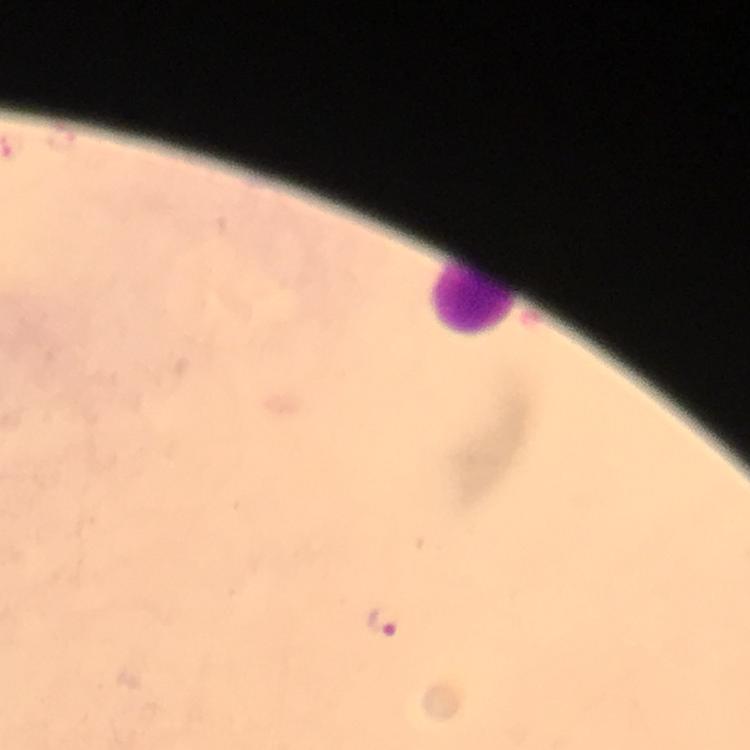

{
  "cropped_from": "one field of view",
  "stain": "Giemsa",
  "context": "from a diagnostic examination for malaria",
  "plasmodium_parasite_locations": "approximate centers as [x, y] in pixels: [385, 622]",
  "leukocyte_locations": "approximate centers as [x, y] in pixels: [473, 297]",
  "magnification": "100x",
  "preparation": "thick smear",
  "capture": "smartphone photograph through a microscope",
  "immersion_oil": "used",
  "image_size": "750×750 pixels"
}